Name the blood parasite species.
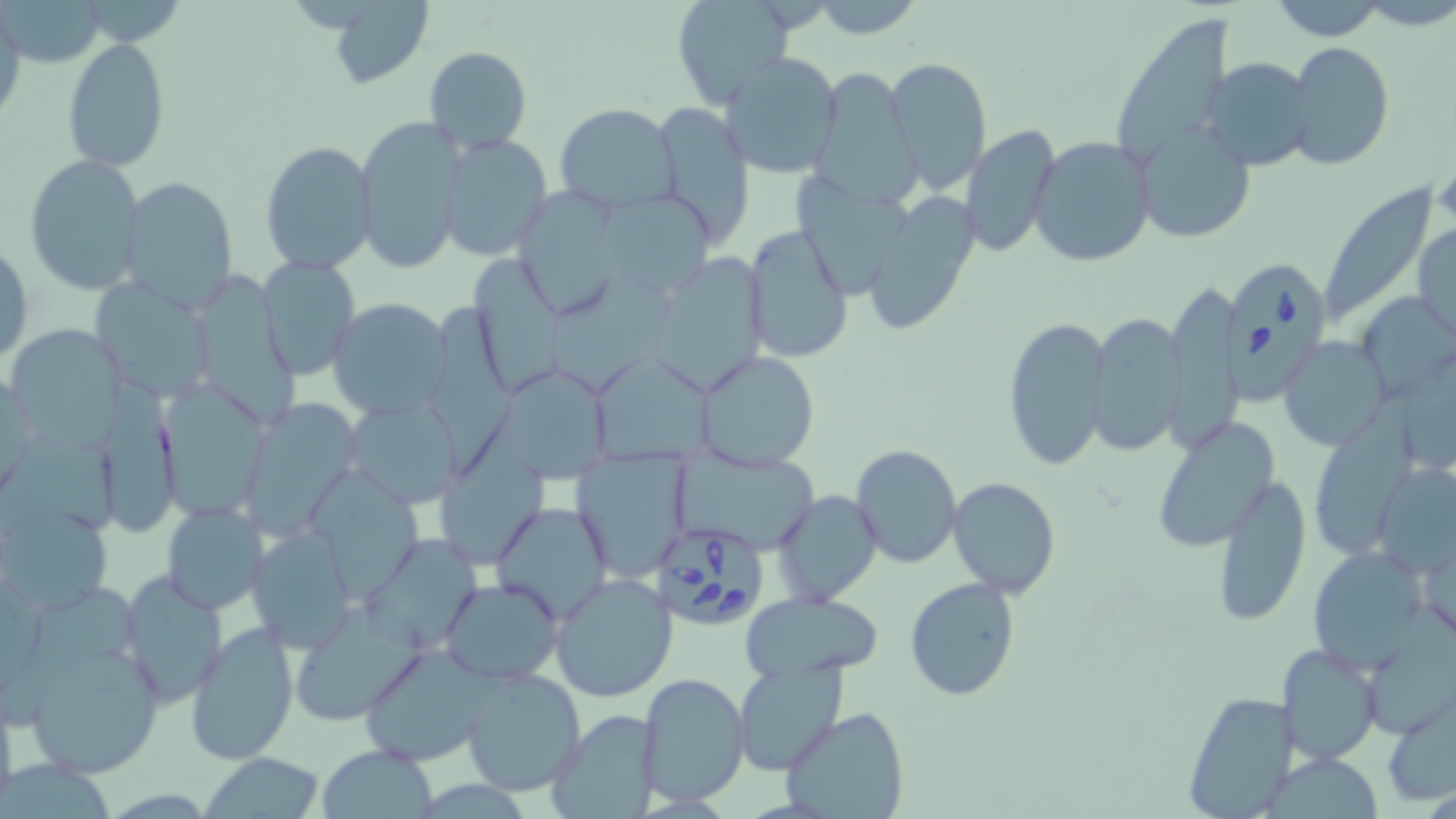

Babesia divergens.

{
  "magnification": "1000x",
  "stain": "May-Grünwald-Giemsa",
  "modality": "optical microscopy",
  "preparation": "thin blood smear",
  "field_of_view": "single",
  "image_size": "1456×819 pixels",
  "babesia_divergens_infected_red_blood_cell_locations": "approximate bounding boxes as named x1/y1/x2/y2 corners in pixels: (x1=1219, y1=255, x2=1336, y2=405), (x1=654, y1=525, x2=765, y2=630)",
  "uninfected_red_blood_cell_locations": "approximate bounding boxes as named x1/y1/x2/y2 corners in pixels: (x1=804, y1=0, x2=925, y2=38), (x1=1264, y1=0, x2=1394, y2=41), (x1=325, y1=1, x2=434, y2=88), (x1=670, y1=1, x2=799, y2=112), (x1=0, y1=8, x2=26, y2=126), (x1=1113, y1=15, x2=1232, y2=165), (x1=63, y1=37, x2=169, y2=171), (x1=1286, y1=41, x2=1394, y2=170), (x1=425, y1=46, x2=530, y2=151), (x1=720, y1=51, x2=844, y2=178), (x1=1204, y1=56, x2=1316, y2=172), (x1=884, y1=57, x2=993, y2=193), (x1=807, y1=69, x2=918, y2=205), (x1=652, y1=100, x2=755, y2=246), (x1=555, y1=104, x2=678, y2=214), (x1=354, y1=116, x2=466, y2=274), (x1=959, y1=123, x2=1061, y2=261), (x1=1135, y1=125, x2=1256, y2=243), (x1=439, y1=133, x2=552, y2=261), (x1=1028, y1=137, x2=1155, y2=268), (x1=260, y1=140, x2=378, y2=272), (x1=23, y1=153, x2=146, y2=295), (x1=797, y1=171, x2=915, y2=309), (x1=118, y1=176, x2=240, y2=313), (x1=513, y1=178, x2=624, y2=324), (x1=1315, y1=180, x2=1437, y2=334), (x1=863, y1=193, x2=984, y2=337), (x1=597, y1=195, x2=721, y2=290), (x1=1414, y1=221, x2=1455, y2=344), (x1=741, y1=223, x2=854, y2=364), (x1=1, y1=243, x2=32, y2=370), (x1=466, y1=250, x2=567, y2=397), (x1=661, y1=253, x2=778, y2=395), (x1=258, y1=254, x2=361, y2=378), (x1=553, y1=267, x2=675, y2=393), (x1=94, y1=280, x2=212, y2=397), (x1=1166, y1=283, x2=1245, y2=445), (x1=1362, y1=289, x2=1456, y2=386), (x1=427, y1=293, x2=514, y2=479), (x1=326, y1=298, x2=451, y2=420), (x1=1087, y1=314, x2=1187, y2=455), (x1=1002, y1=316, x2=1113, y2=472), (x1=11, y1=324, x2=128, y2=454), (x1=1278, y1=338, x2=1389, y2=449), (x1=696, y1=349, x2=821, y2=473), (x1=591, y1=354, x2=720, y2=467), (x1=491, y1=366, x2=616, y2=485), (x1=102, y1=376, x2=190, y2=540), (x1=157, y1=387, x2=267, y2=518), (x1=1311, y1=397, x2=1410, y2=563), (x1=345, y1=398, x2=459, y2=508), (x1=247, y1=399, x2=360, y2=542), (x1=1151, y1=416, x2=1280, y2=552), (x1=438, y1=430, x2=554, y2=559), (x1=9, y1=434, x2=123, y2=540), (x1=850, y1=443, x2=961, y2=570), (x1=570, y1=449, x2=690, y2=579), (x1=671, y1=450, x2=820, y2=546), (x1=1373, y1=462, x2=1456, y2=580), (x1=312, y1=466, x2=419, y2=604), (x1=1212, y1=470, x2=1313, y2=628), (x1=947, y1=477, x2=1061, y2=597), (x1=771, y1=490, x2=882, y2=606), (x1=490, y1=501, x2=613, y2=623), (x1=161, y1=503, x2=267, y2=614), (x1=5, y1=507, x2=109, y2=620), (x1=248, y1=526, x2=359, y2=653), (x1=370, y1=541, x2=489, y2=651), (x1=1309, y1=548, x2=1431, y2=670), (x1=118, y1=572, x2=227, y2=704), (x1=549, y1=573, x2=678, y2=702), (x1=905, y1=577, x2=1021, y2=702), (x1=440, y1=579, x2=562, y2=684), (x1=23, y1=583, x2=150, y2=713), (x1=743, y1=592, x2=884, y2=678), (x1=1365, y1=595, x2=1456, y2=738), (x1=186, y1=622, x2=299, y2=765), (x1=21, y1=637, x2=165, y2=781), (x1=1276, y1=643, x2=1385, y2=765), (x1=359, y1=646, x2=492, y2=766), (x1=733, y1=660, x2=848, y2=777), (x1=459, y1=666, x2=586, y2=795), (x1=637, y1=672, x2=751, y2=805), (x1=1180, y1=689, x2=1302, y2=817), (x1=0, y1=692, x2=19, y2=810), (x1=1381, y1=692, x2=1456, y2=810), (x1=780, y1=706, x2=909, y2=819), (x1=545, y1=709, x2=662, y2=818), (x1=318, y1=745, x2=437, y2=818), (x1=202, y1=752, x2=324, y2=819)"
}